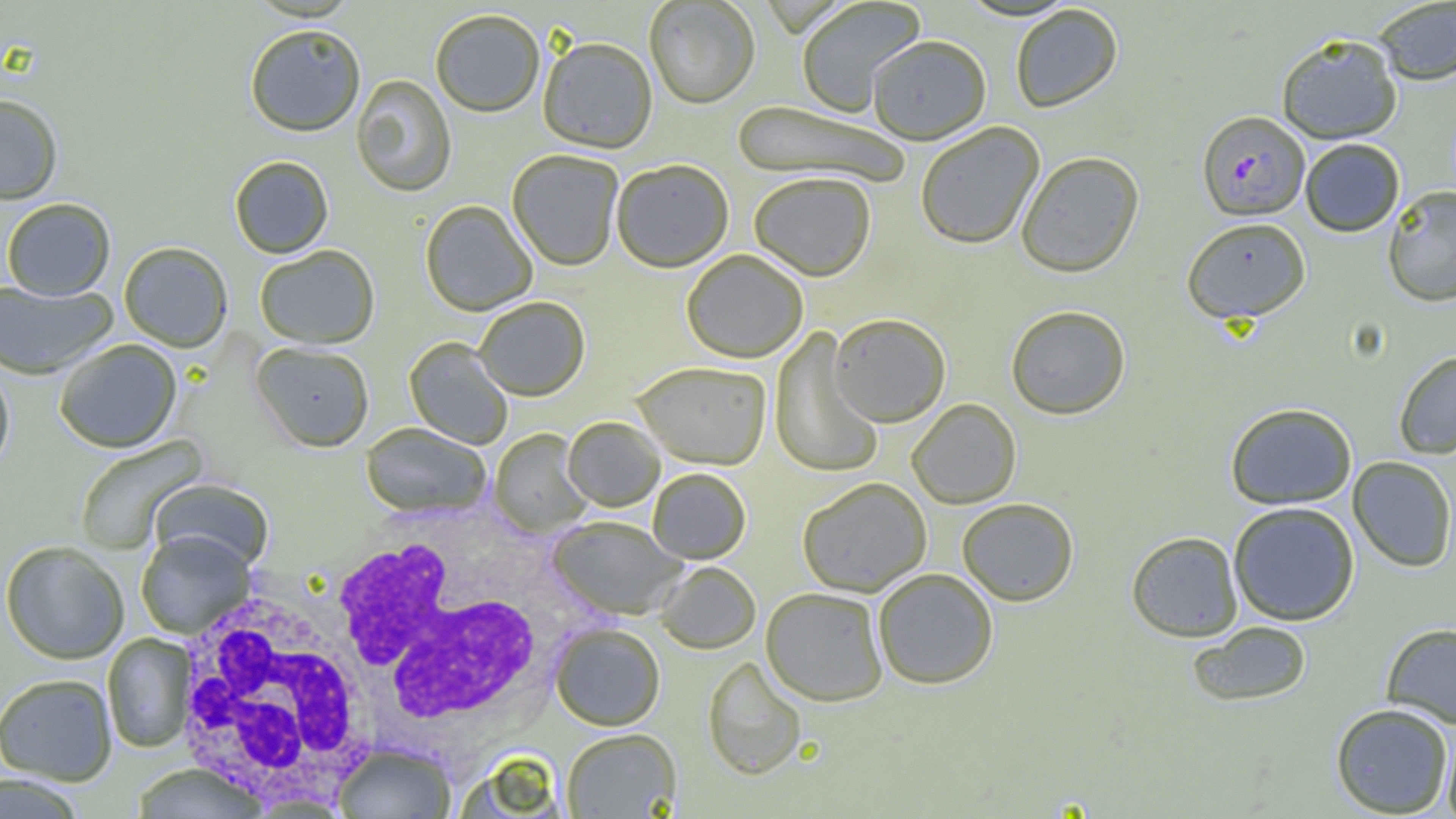
Summary:
  - Coordinate format: approximate bounding boxes as (x1, y1, x2, y2) in pixels
  - Plasmodium falciparum-infected red blood cell locations: (1196, 110, 1310, 220)
  - White blood cell locations: (326, 520, 582, 741), (169, 586, 385, 809)
  - Uninfected red blood cell locations: (795, 0, 926, 117), (644, 1, 760, 110), (1372, 1, 1456, 85), (1010, 4, 1123, 113), (431, 11, 545, 120), (245, 26, 366, 139), (1276, 33, 1403, 144), (867, 36, 991, 145), (537, 40, 657, 155), (351, 76, 457, 198), (0, 96, 62, 206), (732, 102, 910, 189), (915, 122, 1045, 250), (1300, 138, 1405, 237), (507, 151, 623, 272), (1016, 151, 1145, 278), (229, 157, 334, 259), (611, 162, 734, 274), (748, 174, 876, 282), (1382, 186, 1456, 306), (2, 200, 116, 302), (420, 201, 537, 317), (1181, 216, 1311, 323), (119, 243, 233, 353), (255, 246, 380, 350), (681, 250, 809, 364), (0, 281, 116, 380), (475, 298, 590, 402), (1005, 305, 1131, 419), (829, 314, 951, 427), (769, 328, 884, 479), (404, 337, 513, 450), (55, 340, 182, 454), (252, 344, 374, 453), (1393, 349, 1456, 459), (0, 362, 14, 479), (632, 363, 772, 471), (907, 399, 1022, 508), (1225, 402, 1357, 509), (563, 418, 664, 512), (361, 424, 491, 520), (489, 429, 593, 538), (73, 435, 209, 555), (1347, 456, 1456, 572), (648, 469, 751, 565), (797, 478, 932, 597), (150, 480, 274, 572), (957, 498, 1079, 606), (1227, 501, 1360, 626), (548, 516, 686, 620), (1125, 530, 1244, 642), (136, 531, 255, 639), (0, 542, 129, 665), (655, 562, 761, 655), (873, 569, 999, 690), (761, 588, 888, 706), (1186, 621, 1313, 707), (1381, 622, 1456, 728), (550, 624, 665, 732), (103, 634, 196, 753), (702, 657, 807, 781), (0, 675, 117, 786), (1330, 702, 1454, 817), (1441, 723, 1456, 819), (561, 729, 682, 819), (332, 743, 457, 818), (454, 750, 570, 819), (130, 764, 270, 818), (1, 774, 86, 819)
  - Slide-level diagnosis: Plasmodium falciparum
  - Field of view: one of a larger specimen
  - Image size: 1456×819 pixels
  - Magnification: 1000x
  - Preparation: thin blood film
  - Modality: optical microscopy